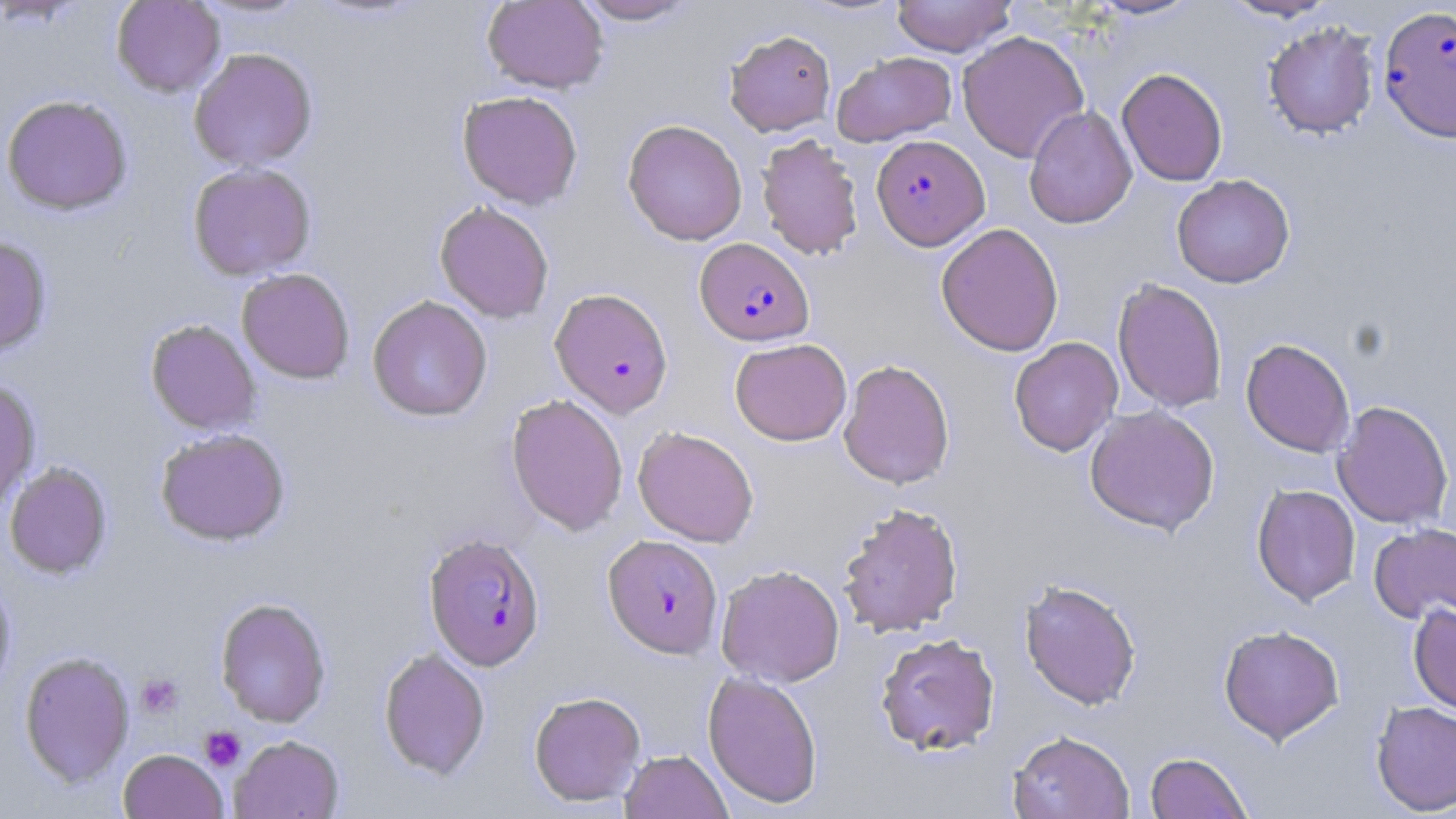
slide-level diagnosis = Plasmodium falciparum
magnification = 1000x
preparation = thin blood film
uninfected red blood cell locations = approximate bounding boxes as named x1/y1/x2/y2 corners in pixels: (x1=111, y1=0, x2=225, y2=97), (x1=192, y1=0, x2=314, y2=20), (x1=482, y1=0, x2=608, y2=94), (x1=574, y1=0, x2=701, y2=25), (x1=891, y1=0, x2=1016, y2=57), (x1=1083, y1=0, x2=1204, y2=20), (x1=1219, y1=0, x2=1338, y2=22), (x1=1263, y1=22, x2=1380, y2=139), (x1=725, y1=29, x2=836, y2=136), (x1=956, y1=30, x2=1089, y2=162), (x1=188, y1=47, x2=318, y2=171), (x1=832, y1=51, x2=957, y2=146), (x1=1117, y1=68, x2=1228, y2=186), (x1=457, y1=90, x2=583, y2=209), (x1=1, y1=95, x2=133, y2=215), (x1=1024, y1=106, x2=1137, y2=229), (x1=622, y1=119, x2=748, y2=246), (x1=756, y1=133, x2=864, y2=261), (x1=188, y1=162, x2=316, y2=280), (x1=1172, y1=174, x2=1295, y2=288), (x1=435, y1=200, x2=554, y2=323), (x1=936, y1=222, x2=1064, y2=356), (x1=0, y1=235, x2=52, y2=358), (x1=236, y1=268, x2=355, y2=384), (x1=1113, y1=278, x2=1227, y2=413), (x1=367, y1=295, x2=492, y2=422), (x1=145, y1=319, x2=262, y2=435), (x1=1009, y1=337, x2=1123, y2=456), (x1=730, y1=338, x2=852, y2=446), (x1=1241, y1=338, x2=1355, y2=457), (x1=838, y1=358, x2=955, y2=490), (x1=0, y1=380, x2=41, y2=513), (x1=505, y1=394, x2=628, y2=536), (x1=1333, y1=400, x2=1453, y2=529), (x1=1084, y1=404, x2=1220, y2=536), (x1=633, y1=426, x2=759, y2=547), (x1=155, y1=428, x2=290, y2=546), (x1=3, y1=462, x2=113, y2=579), (x1=1252, y1=483, x2=1360, y2=606), (x1=837, y1=502, x2=964, y2=638), (x1=1369, y1=522, x2=1456, y2=626), (x1=715, y1=564, x2=845, y2=687), (x1=0, y1=578, x2=16, y2=695), (x1=1019, y1=578, x2=1142, y2=710), (x1=215, y1=597, x2=331, y2=728), (x1=1408, y1=603, x2=1456, y2=715), (x1=1218, y1=624, x2=1344, y2=744), (x1=875, y1=632, x2=1001, y2=756), (x1=378, y1=647, x2=491, y2=779), (x1=19, y1=651, x2=134, y2=787), (x1=702, y1=670, x2=823, y2=809), (x1=529, y1=690, x2=646, y2=806), (x1=1371, y1=700, x2=1456, y2=815), (x1=1007, y1=729, x2=1135, y2=819), (x1=230, y1=734, x2=344, y2=819), (x1=118, y1=749, x2=229, y2=819), (x1=620, y1=749, x2=733, y2=819), (x1=1145, y1=752, x2=1253, y2=819)
Plasmodium falciparum-infected red blood cell locations = approximate bounding boxes as named x1/y1/x2/y2 corners in pixels: (x1=1378, y1=5, x2=1456, y2=143), (x1=871, y1=135, x2=989, y2=250), (x1=694, y1=237, x2=814, y2=346), (x1=550, y1=288, x2=674, y2=417), (x1=423, y1=532, x2=545, y2=670), (x1=603, y1=534, x2=723, y2=658)
modality = optical microscopy
image size = 1456×819 pixels
stain = May-Grünwald-Giemsa
field of view = single
platelet locations = approximate bounding boxes as named x1/y1/x2/y2 corners in pixels: (x1=136, y1=674, x2=184, y2=719), (x1=199, y1=726, x2=246, y2=772)